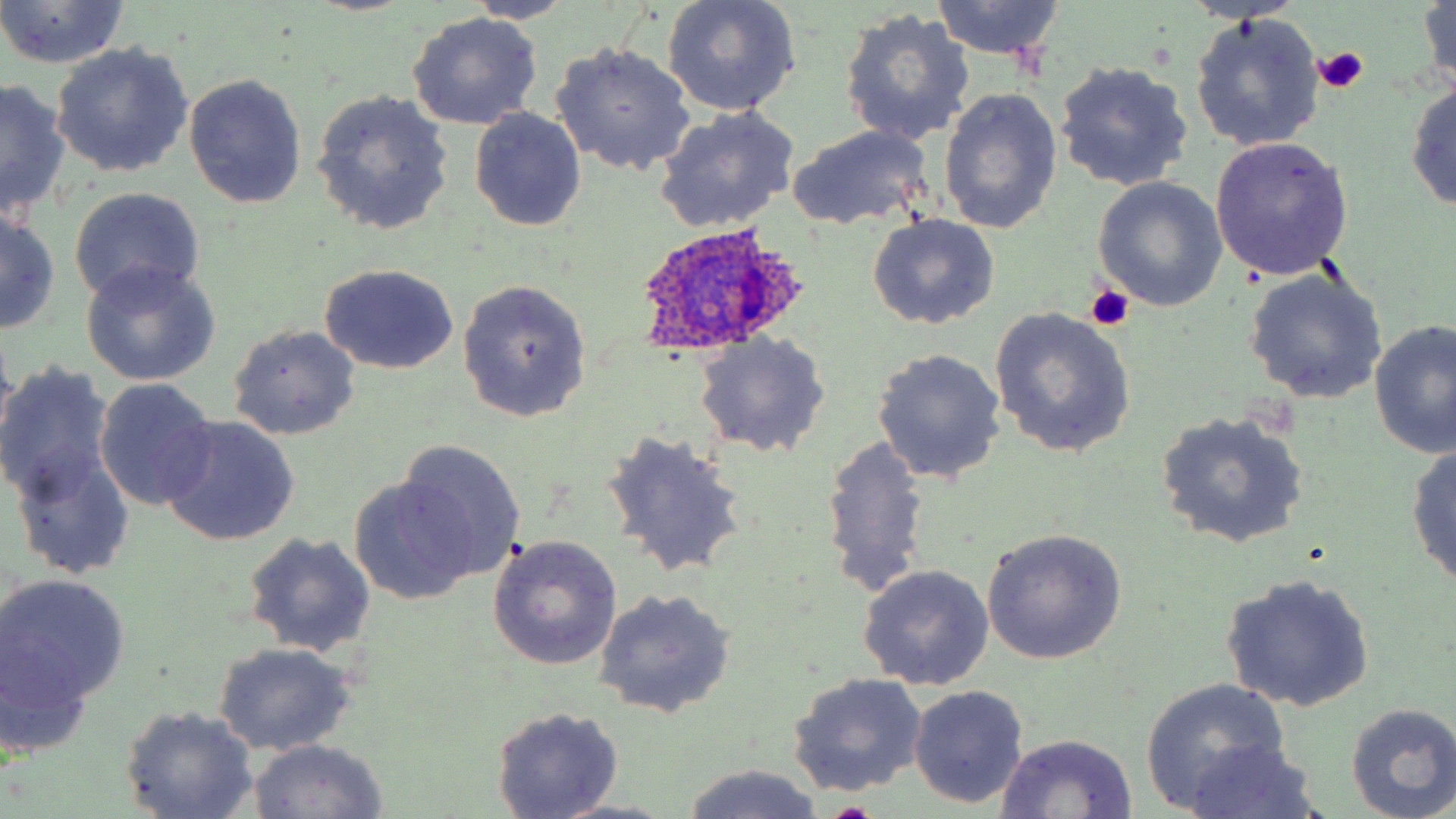
Approximate bounding boxes as [x1, y1, x2, y2] in pixels. Platelet locations: [1313, 45, 1368, 92], [1086, 284, 1134, 331]. Plasmodium ovale-infected red blood cell locations: [629, 223, 812, 356]. Uninfected red blood cell locations: [464, 0, 579, 24], [661, 0, 802, 116], [1417, 0, 1454, 96], [930, 1, 1066, 60], [0, 2, 130, 69], [839, 7, 975, 148], [407, 12, 544, 130], [1189, 13, 1326, 153], [49, 43, 194, 179], [552, 43, 696, 176], [1054, 61, 1194, 194], [183, 73, 307, 209], [1406, 76, 1456, 215], [1, 80, 71, 223], [311, 89, 454, 237], [940, 89, 1062, 235], [655, 105, 802, 232], [469, 107, 587, 232], [787, 125, 933, 231], [1209, 135, 1355, 279], [1092, 177, 1227, 311], [68, 187, 206, 306], [0, 210, 60, 334], [867, 214, 1000, 329], [81, 263, 220, 385], [320, 265, 459, 375], [1243, 266, 1387, 405], [456, 280, 592, 422], [990, 308, 1136, 458], [1370, 319, 1456, 459], [229, 325, 360, 439], [693, 332, 830, 458], [871, 348, 1007, 484], [0, 366, 115, 508], [93, 379, 219, 511], [1155, 411, 1310, 550], [157, 416, 300, 547], [601, 430, 749, 580], [819, 435, 933, 600], [394, 439, 528, 581], [1406, 441, 1456, 592], [12, 443, 135, 580], [348, 478, 475, 601], [983, 528, 1127, 666], [243, 532, 376, 657], [487, 535, 623, 670], [857, 564, 994, 690], [1220, 573, 1376, 712], [0, 574, 130, 711], [593, 588, 735, 717], [211, 641, 358, 755], [787, 672, 927, 797], [1141, 679, 1291, 811], [908, 685, 1030, 810], [1346, 703, 1456, 818], [120, 706, 259, 818], [491, 706, 623, 818], [995, 733, 1138, 817], [246, 740, 391, 819], [1178, 740, 1324, 818], [676, 763, 834, 819], [551, 799, 678, 819]. Slide-level diagnosis: Plasmodium ovale. Captured at 1000x magnification. May-Grünwald-Giemsa stain. Light microscopy. Single field of view. Image is 1456×819 pixels. Thin blood smear.